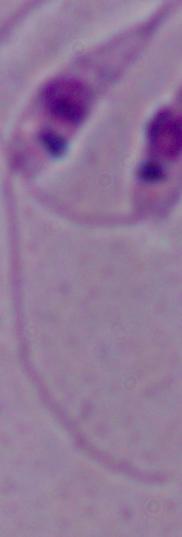

Summary:
  - Identification: Leishmania
  - Modality: photomicrograph
  - Magnification: 1000x